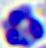

magnification = 400x
identification = leukocyte
modality = micrograph